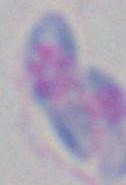
{
  "identification": "Toxoplasma gondii",
  "modality": "photomicrograph",
  "magnification": "1000x"
}